Locate every Plasmodium parasite.
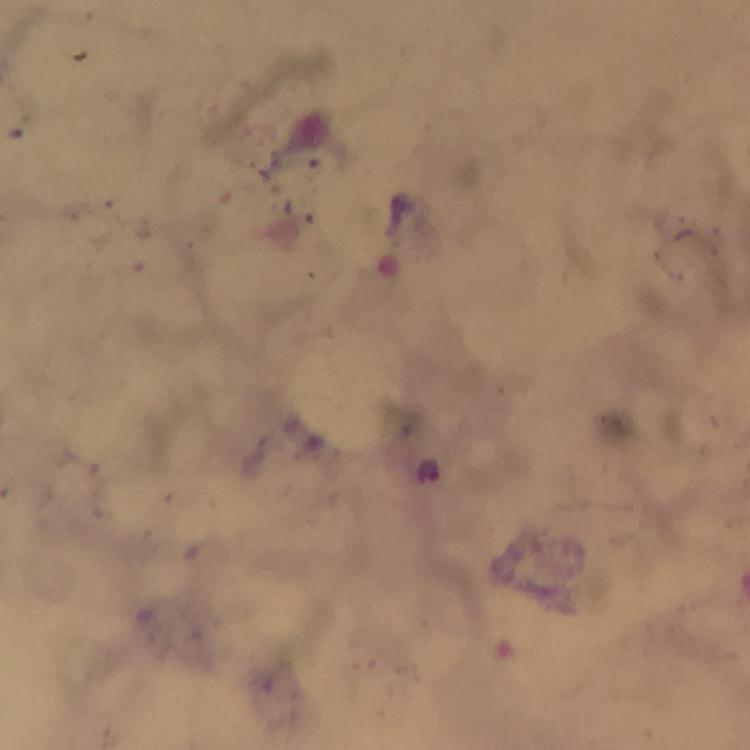

Approximate centers as [x, y] in pixels.
Plasmodium parasites: [427, 470].

Summary:
  - Stain: Giemsa
  - Magnification: 100x
  - Image size: 750×750 pixels
  - Cropped from: one field of view
  - Immersion oil: used
  - Capture: smartphone camera through the microscope
  - Context: from a malaria diagnostic workup
  - Preparation: thick smear